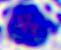

identification = white blood cell
magnification = 400x
modality = micrograph